Classify this cell by malaria status.
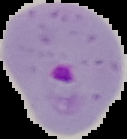
Parasitized.

image size = 127×139 pixels
image type = segmented cell region with the area outside set to black
preparation = thin blood smear